Locate the red blood cells and classify each one as Plasmodium falciparum-infected, uninfected, or of indeterminate infection status.
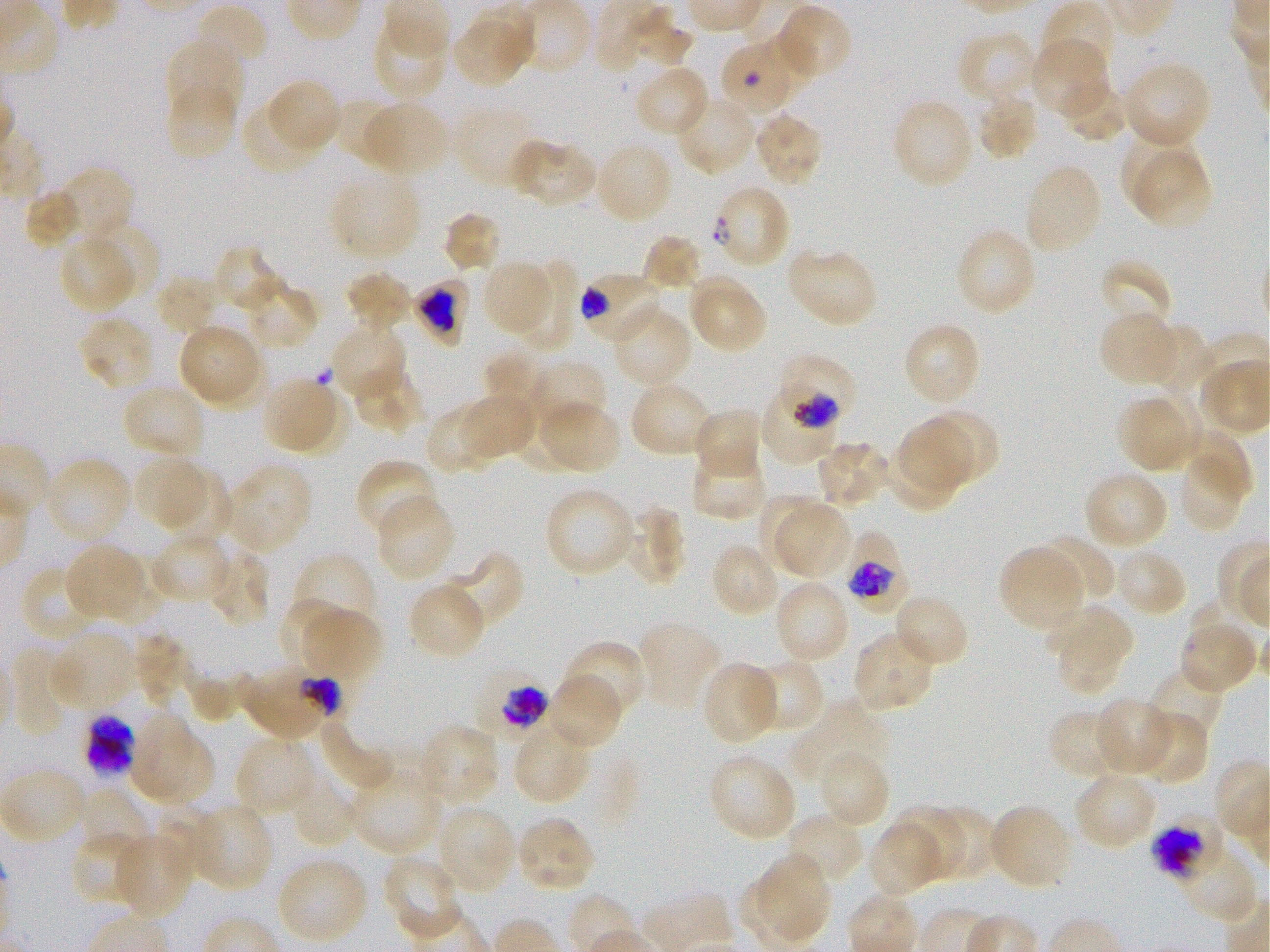
Approximate bounding boxes as (x1, y1, x2, y2) in pixels. Not every red blood cell is marked. A life-cycle stage — or a range of stages, where the recorded stages span more than one — follows each staged infected red blood cell.
Infected red blood cells: (721, 47, 789, 109); (711, 183, 791, 269); (579, 269, 665, 346) early trophozoite; (411, 277, 472, 347) late trophozoite to early schizont; (778, 357, 858, 425) early trophozoite to early schizont; (843, 531, 904, 604) late trophozoite to late schizont; (476, 664, 554, 742) late trophozoite to early schizont; (1149, 809, 1226, 881) early schizont.
Red blood cells of indeterminate infection status: (769, 386, 837, 468), (240, 662, 344, 742), (85, 716, 134, 778).
Uninfected red blood cells: (1040, 1, 1117, 78), (773, 2, 853, 83), (193, 3, 271, 70), (371, 17, 448, 101), (452, 21, 527, 88), (757, 31, 816, 93), (955, 31, 1039, 105), (165, 38, 244, 120), (1029, 38, 1110, 120), (1122, 60, 1213, 149), (633, 64, 710, 138), (1057, 75, 1130, 143), (264, 78, 343, 157), (165, 80, 239, 162), (975, 91, 1039, 161), (675, 95, 757, 175), (333, 96, 406, 168), (891, 97, 975, 190), (240, 98, 324, 175), (366, 100, 450, 171), (454, 106, 540, 190), (752, 110, 825, 186), (1121, 124, 1197, 207), (509, 136, 599, 209), (593, 141, 674, 224), (1136, 153, 1213, 228), (1024, 162, 1104, 256), (58, 170, 134, 248), (329, 172, 422, 262), (25, 190, 83, 248), (441, 209, 502, 273), (98, 218, 165, 291), (955, 228, 1037, 318), (57, 233, 139, 314), (643, 234, 702, 291), (786, 245, 879, 329), (216, 248, 286, 312), (480, 260, 556, 337), (1099, 260, 1172, 333), (512, 262, 580, 354), (347, 271, 414, 332), (687, 272, 768, 356), (157, 275, 223, 335), (238, 279, 318, 350), (611, 306, 693, 389), (1099, 310, 1181, 388), (78, 315, 157, 393), (329, 321, 408, 401), (178, 322, 267, 410), (902, 322, 982, 408), (1139, 324, 1213, 394), (485, 350, 552, 414), (529, 360, 607, 424), (351, 364, 424, 435), (261, 376, 335, 451), (629, 381, 716, 458), (120, 383, 207, 460), (276, 390, 348, 455), (1133, 391, 1203, 470), (454, 394, 537, 463), (1114, 396, 1186, 470), (534, 399, 622, 475), (513, 402, 582, 472), (426, 404, 505, 471), (692, 407, 765, 481), (927, 412, 999, 484), (898, 420, 971, 492), (1183, 428, 1252, 501), (815, 439, 892, 509), (887, 442, 957, 513), (688, 447, 770, 521), (132, 454, 213, 532), (42, 456, 133, 547), (1182, 456, 1240, 528), (355, 458, 440, 539), (220, 462, 312, 555), (1082, 469, 1169, 551), (161, 470, 233, 543), (544, 486, 637, 579), (375, 494, 457, 583), (759, 494, 834, 569), (776, 504, 852, 578), (627, 505, 686, 586), (149, 531, 234, 605), (1034, 534, 1116, 604), (64, 543, 149, 623), (708, 543, 781, 618), (205, 546, 270, 628), (998, 546, 1087, 634), (1112, 547, 1188, 618), (441, 549, 525, 630), (292, 552, 379, 640), (21, 565, 102, 643), (773, 579, 851, 665), (408, 580, 487, 660), (892, 592, 970, 669), (295, 602, 383, 680), (1049, 604, 1136, 671), (1177, 617, 1259, 695), (636, 619, 723, 711), (49, 626, 139, 713), (852, 630, 938, 714), (132, 631, 194, 711), (1056, 632, 1117, 694), (560, 640, 648, 723), (13, 645, 74, 735), (744, 659, 827, 735), (701, 660, 780, 746), (1147, 666, 1225, 742), (545, 671, 623, 751), (1094, 697, 1174, 775), (792, 701, 885, 785), (1047, 709, 1129, 780), (1135, 709, 1210, 786), (130, 711, 216, 808), (513, 717, 594, 806), (316, 718, 397, 794), (413, 723, 499, 810), (234, 734, 318, 818), (817, 749, 890, 830), (706, 752, 798, 843), (1, 766, 89, 845), (348, 769, 445, 857), (289, 770, 358, 849), (1073, 771, 1159, 851), (77, 786, 149, 860), (188, 802, 273, 892), (987, 802, 1074, 891), (434, 804, 517, 896), (892, 804, 969, 879), (931, 809, 999, 880), (782, 812, 865, 889), (514, 814, 597, 893), (867, 820, 948, 898), (70, 830, 152, 907), (111, 830, 194, 919), (1172, 845, 1259, 923), (757, 853, 832, 937), (381, 856, 464, 943), (275, 857, 368, 947).

Summary:
  - Image size: 1270×952 pixels
  - Life-cycle stages observed: trophozoite, schizont
  - Culture: in-vitro Plasmodium falciparum strain 3D7, static
  - Donor blood group: O+
  - Objective: 100x, oil immersion, numerical aperture 1.25
  - Field of view: one from this slide
  - Preparation: thin blood smear
  - Stain: Giemsa